Locate every blood parasite and identify its species.
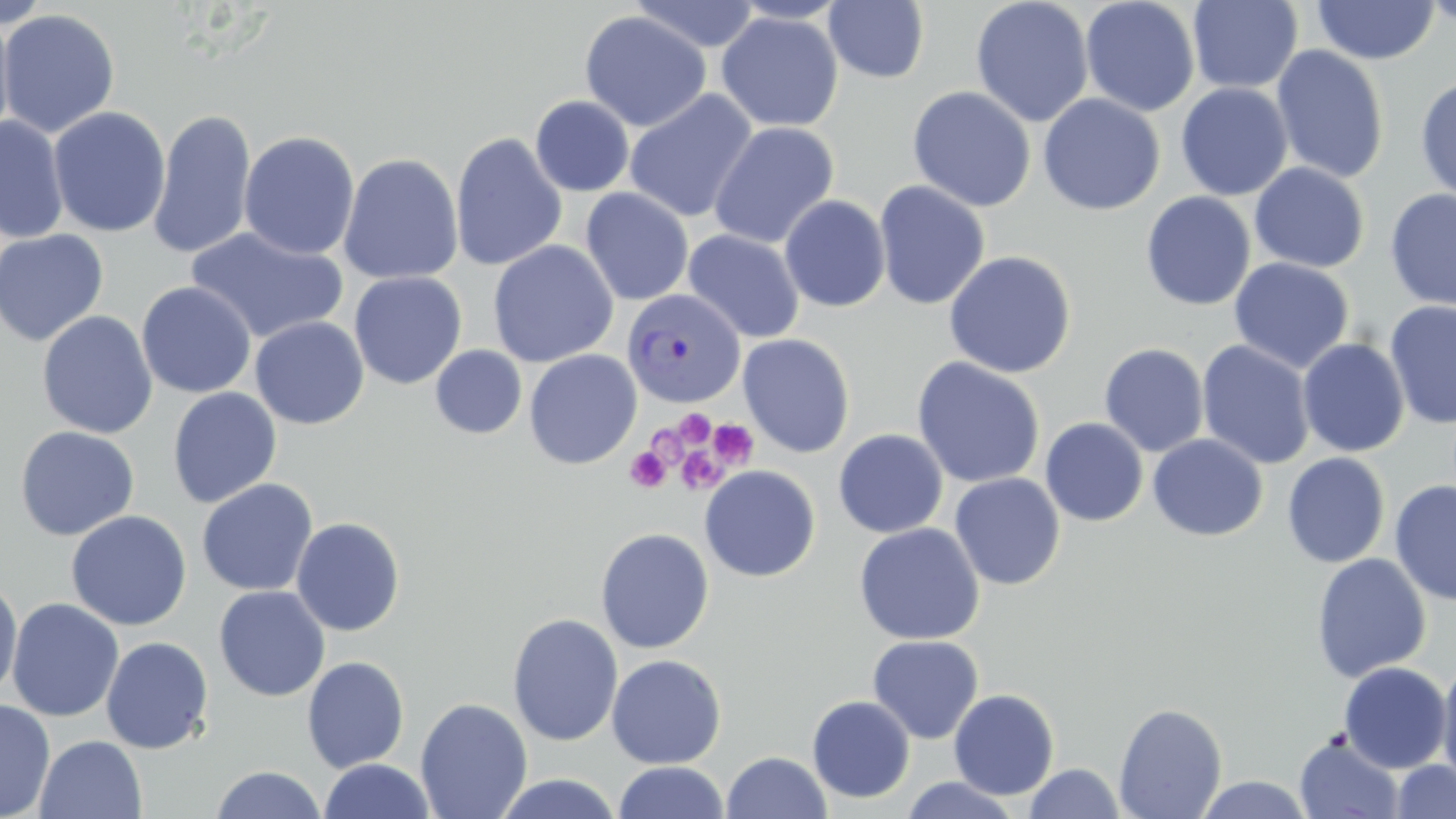
Approximate bounding boxes as (x1,y1)-(x2,y2) corner pairs in pixels.
Plasmodium vivax-infected red blood cells: (623,289)-(746,409).
No Plasmodium falciparum, Plasmodium ovale, Plasmodium malariae, Babesia divergens, or Trypanosoma brucei observed.

Platelet locations: (674,409)-(715,449), (708,418)-(759,470), (625,447)-(670,493), (676,447)-(725,495). Uninfected red blood cell locations: (629,0)-(762,53), (1080,0)-(1200,117), (1420,0)-(1456,30), (1,1)-(54,29), (728,1)-(850,24), (823,1)-(930,84), (970,1)-(1094,128), (1187,1)-(1304,94), (1310,1)-(1442,65), (0,9)-(120,139), (579,10)-(712,132), (716,11)-(843,133), (0,12)-(17,145), (1270,45)-(1390,184), (1415,75)-(1456,203), (1175,82)-(1294,201), (907,86)-(1036,212), (624,89)-(758,223), (1038,94)-(1165,216), (530,95)-(634,197), (47,106)-(171,238), (147,108)-(257,260), (0,115)-(69,243), (708,121)-(839,249), (239,130)-(360,260), (450,132)-(568,271), (338,152)-(464,285), (1249,162)-(1370,273), (874,180)-(990,310), (580,187)-(694,305), (1384,188)-(1456,311), (1141,191)-(1257,311), (779,195)-(891,313), (186,226)-(348,345), (0,228)-(109,347), (683,229)-(805,344), (488,239)-(619,368), (944,250)-(1076,378), (1229,257)-(1354,373), (349,271)-(467,390), (136,281)-(257,398), (1384,300)-(1456,429), (37,310)-(158,439), (249,316)-(369,430), (737,333)-(855,458), (1297,337)-(1410,457), (1197,340)-(1316,470), (1099,343)-(1209,457), (430,345)-(527,439), (524,349)-(642,469), (911,357)-(1046,488), (167,387)-(282,509), (1040,418)-(1148,526), (15,425)-(139,541), (833,429)-(948,538), (1148,434)-(1268,541), (1282,452)-(1390,568), (699,465)-(821,583), (949,473)-(1065,590), (197,478)-(318,596), (1390,479)-(1456,607), (66,510)-(192,631), (291,516)-(406,636), (854,522)-(984,645), (594,528)-(715,654), (1311,552)-(1432,682), (0,574)-(23,704), (213,585)-(330,702), (6,597)-(124,722), (507,613)-(624,747), (867,635)-(984,744), (100,636)-(214,754), (606,654)-(727,769), (302,656)-(409,772), (1436,657)-(1456,790), (1338,662)-(1453,773), (948,688)-(1060,800), (807,695)-(915,803), (415,697)-(532,819), (0,699)-(55,819), (1114,702)-(1228,818), (1294,734)-(1405,819), (34,735)-(147,819), (722,751)-(832,819), (318,759)-(436,818), (1391,760)-(1456,818), (612,761)-(729,819), (1023,763)-(1126,818), (209,766)-(328,819), (492,772)-(623,818), (1193,774)-(1316,818), (900,775)-(1022,818). Slide-level diagnosis: Plasmodium vivax. Thin blood film. One field of a larger specimen. Captured at 1000x magnification. May-Grünwald-Giemsa stain. Image is 1456×819 pixels. Optical microscopy.